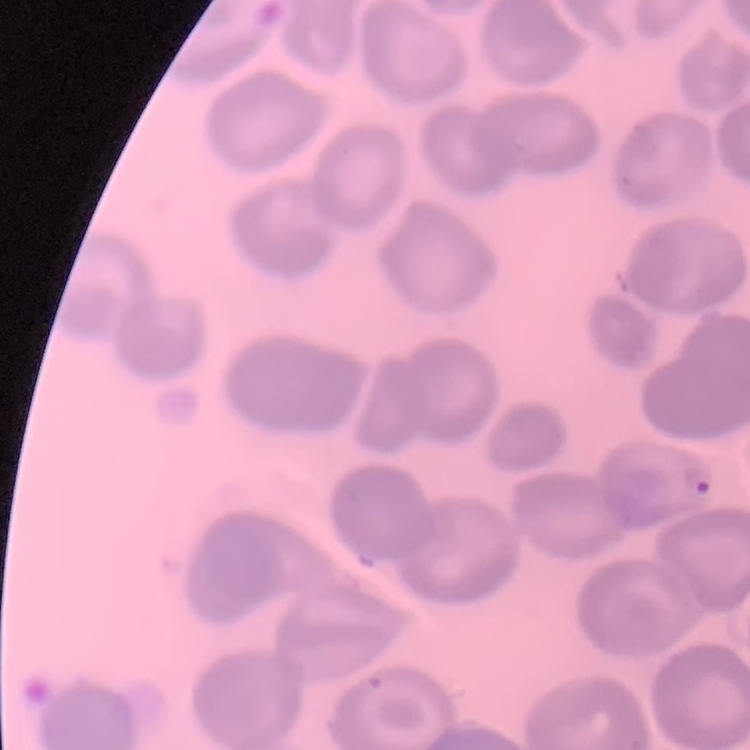
Summary:
  - Red blood cell morphology: no rouleaux formation
  - Preparation: thin blood film
  - Image type: one tile cut from a larger photomicrograph
  - Stain: Field's or Giemsa